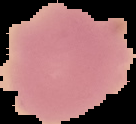
malaria_status: uninfected
image_size: 136×124 pixels
preparation: thin blood smear
image_type: segmented cell region on a black background